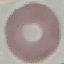
malaria_status: uninfected
capture: smartphone camera at the microscope eyepiece
image_type: cell patch, automatically extracted from a larger field of view and resized to 64 × 64 pixels
stain: Giemsa
preparation: thin blood smear